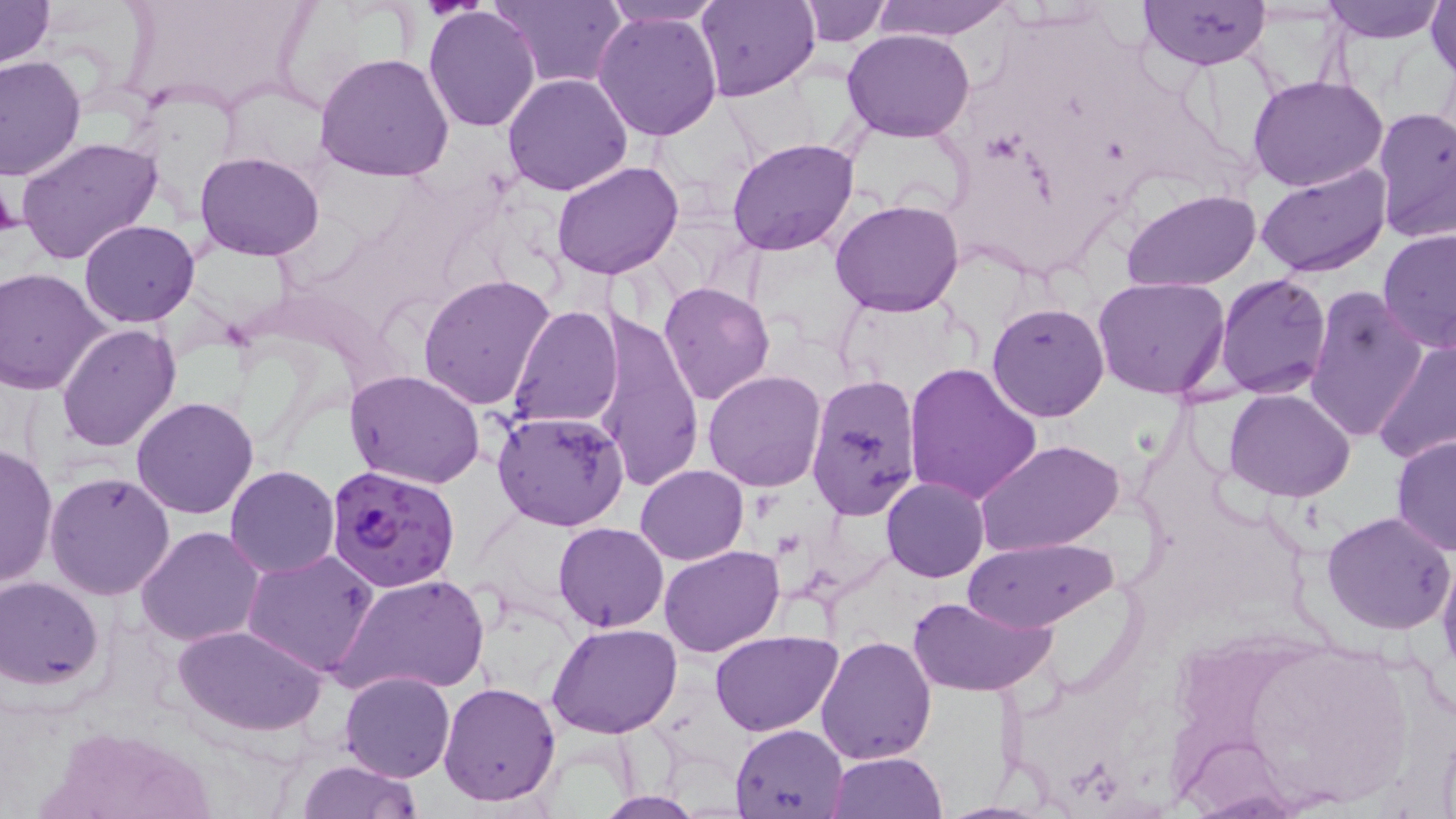
{
  "slide_level_diagnosis": "Plasmodium falciparum",
  "field_of_view": "single",
  "plasmodium_falciparum_infected_red_blood_cell_locations": "approximate bounding boxes as (x1,y1)-(x2,y2) corner pairs in pixels: (324,465)-(462,592)",
  "modality": "optical microscopy",
  "preparation": "thin blood film",
  "platelet_locations": "approximate bounding boxes as (x1,y1)-(x2,y2) corner pairs in pixels: (0,177)-(19,242)",
  "uninfected_red_blood_cell_locations": "approximate bounding boxes as (x1,y1)-(x2,y2) corner pairs in pixels: (0,0)-(54,70), (491,0)-(624,89), (599,0)-(729,28), (695,0)-(818,101), (797,0)-(892,44), (869,0)-(1015,43), (1139,0)-(1271,70), (1322,0)-(1446,43), (1428,0)-(1456,83), (423,6)-(541,132), (592,10)-(724,142), (843,28)-(976,143), (0,53)-(85,182), (314,53)-(454,182), (502,72)-(634,195), (1247,73)-(1389,190), (1373,108)-(1455,245), (15,136)-(161,266), (726,137)-(859,257), (195,151)-(325,260), (551,160)-(683,281), (1256,164)-(1394,278), (1123,190)-(1261,290), (830,200)-(964,318), (80,220)-(200,326), (1378,228)-(1456,355), (2,266)-(113,396), (1214,273)-(1331,397), (418,274)-(556,410), (1092,277)-(1232,400), (659,281)-(773,404), (1304,283)-(1428,446), (985,302)-(1110,422), (508,304)-(622,429), (591,310)-(705,495), (56,323)-(181,451), (1371,334)-(1456,465), (902,363)-(1042,504), (346,370)-(485,490), (702,370)-(827,491), (806,374)-(924,524), (1225,389)-(1355,501), (130,396)-(259,519), (491,409)-(628,532), (1391,433)-(1456,558), (974,438)-(1124,557), (0,442)-(58,588), (635,464)-(748,565), (226,466)-(340,580), (45,472)-(175,600), (881,476)-(988,583), (1321,511)-(1454,635), (554,523)-(669,632), (136,525)-(264,646), (963,537)-(1114,632), (659,545)-(784,658), (242,548)-(381,678), (1436,548)-(1456,672), (336,572)-(486,701), (1,578)-(104,690), (908,594)-(1058,698), (548,621)-(682,738), (171,622)-(326,735), (709,630)-(842,736), (814,635)-(936,766), (1224,636)-(1419,810), (339,671)-(454,783), (439,681)-(565,807), (731,722)-(848,817), (827,749)-(946,819), (296,758)-(424,817), (595,792)-(710,818)",
  "image_size": "1456×819 pixels",
  "stain": "May-Grünwald-Giemsa",
  "magnification": "1000x"
}